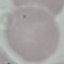

result = no malaria parasites detected
preparation = thin blood smear
image type = cell patch, automatically extracted from a larger field of view and resized to 64 × 64 pixels
capture = smartphone camera at the microscope eyepiece
stain = Giemsa